Locate every malaria parasite and every leukocyte.
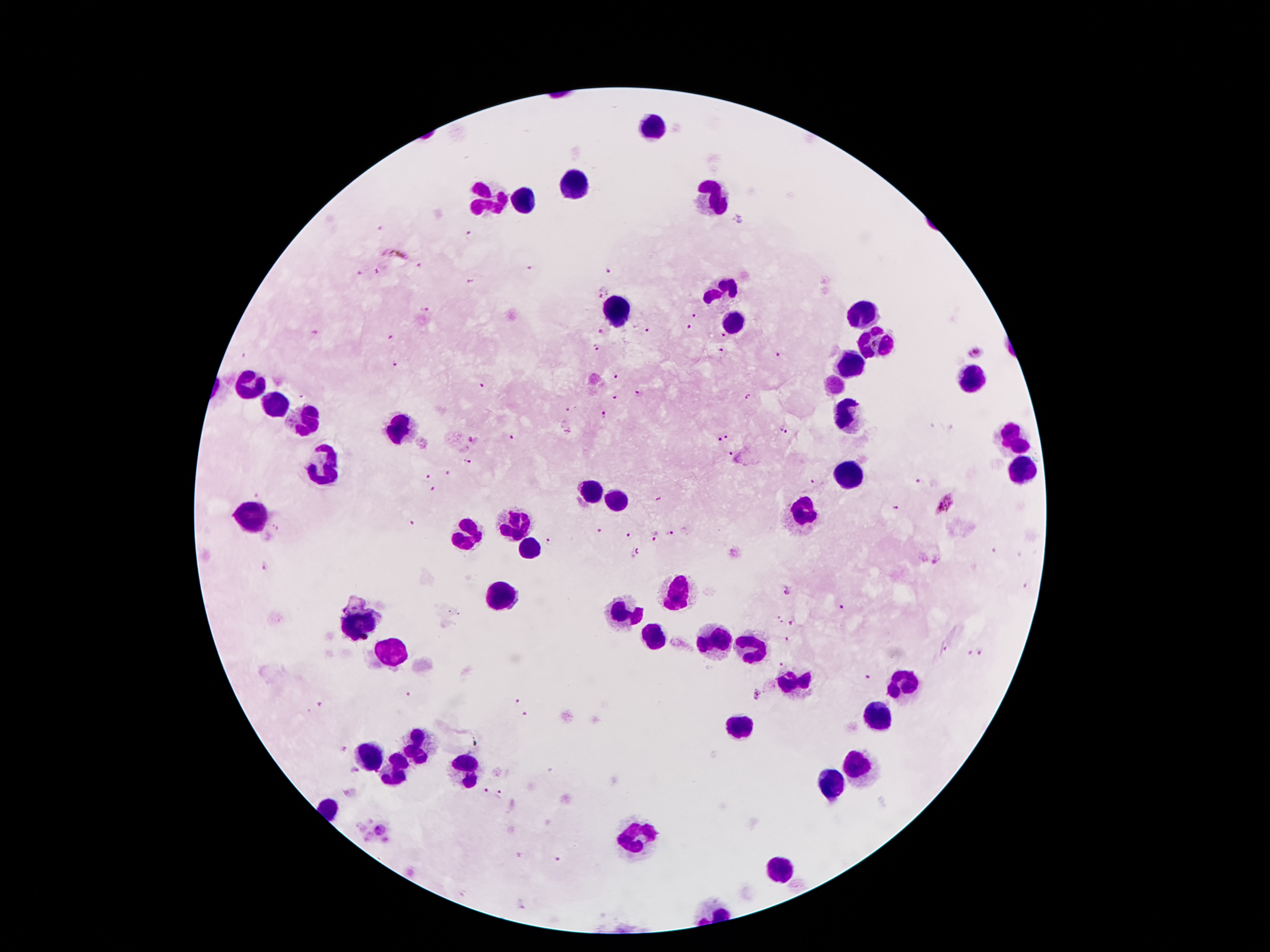

Approximate centers as [x, y] in pixels.
Malaria parasites: [381, 227], [469, 235], [395, 254], [420, 265], [528, 269], [380, 271], [610, 272], [357, 275], [470, 281], [600, 293], [426, 309], [694, 316], [688, 327], [647, 331], [600, 332], [314, 335], [723, 335], [392, 336], [594, 348], [721, 351], [976, 353], [243, 355], [778, 355], [395, 364], [616, 376], [480, 387], [640, 394], [614, 397], [748, 397], [303, 398], [568, 411], [605, 414], [782, 430], [728, 436], [513, 439], [719, 439], [476, 441], [730, 454], [466, 463], [448, 474], [427, 476], [814, 483], [917, 483], [434, 490], [254, 494], [658, 499], [943, 505], [897, 509], [412, 524], [276, 528], [599, 532], [670, 534], [629, 535], [656, 536], [549, 541], [993, 551], [636, 554], [937, 561], [265, 570], [787, 589], [842, 607], [777, 620], [793, 624], [787, 640], [946, 650], [967, 654], [982, 654], [782, 666], [866, 677], [409, 694], [758, 694], [518, 701], [321, 703], [524, 715], [342, 751], [355, 773], [486, 792], [502, 794], [380, 829], [560, 862], [523, 904].
Leukocytes: [651, 124], [572, 187], [527, 201], [713, 202], [488, 205], [720, 291], [617, 312], [858, 314], [735, 322], [880, 341], [855, 364], [971, 380], [250, 389], [277, 409], [849, 420], [307, 423], [399, 427], [1014, 440], [1021, 468], [327, 469], [849, 475], [588, 491], [615, 501], [803, 515], [256, 521], [517, 524], [470, 535], [529, 549], [502, 593], [683, 595], [620, 613], [359, 627], [654, 641], [713, 643], [749, 649], [392, 656], [903, 685], [796, 688], [878, 714], [737, 732], [417, 749], [368, 759], [863, 763], [468, 771], [393, 772], [833, 784], [633, 837], [781, 870].

Single field of view. 100x magnification. Thick blood film. Patient malaria status: positive for Plasmodium falciparum. Smartphone photograph taken through the microscope eyepiece. Giemsa stain. Image is 1270×952 pixels.